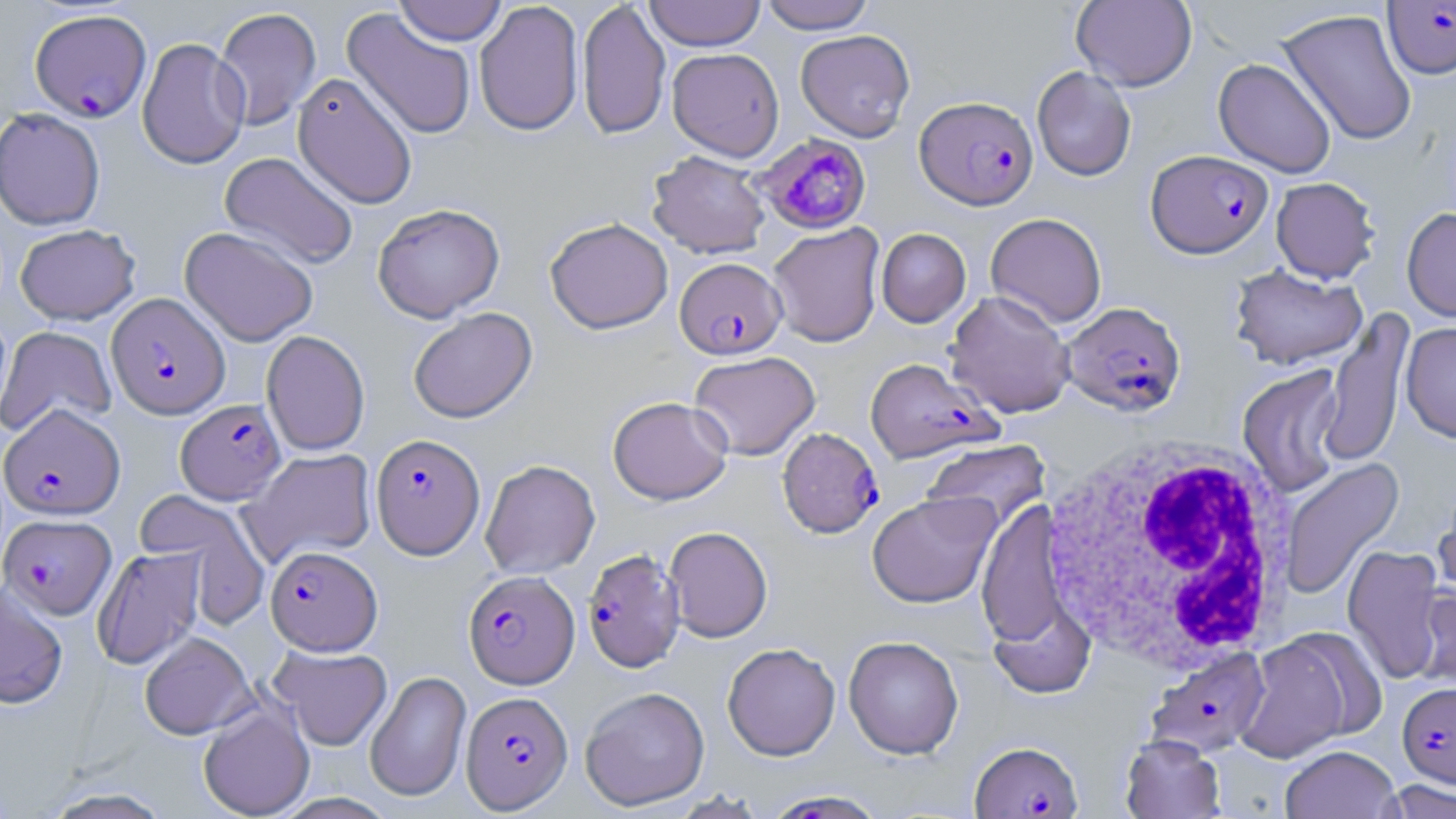 Approximate bounding boxes as [x1, y1, x2, y2] in pixels. White blood cell locations: [1038, 435, 1301, 678]. Uninfected red blood cell locations: [393, 0, 508, 46], [577, 0, 671, 140], [644, 0, 765, 51], [1071, 0, 1198, 91], [759, 1, 876, 33], [473, 2, 583, 137], [213, 6, 322, 131], [341, 7, 477, 140], [1277, 9, 1418, 147], [795, 29, 914, 142], [136, 37, 250, 169], [667, 48, 784, 161], [1214, 58, 1336, 177], [1032, 66, 1136, 181], [292, 72, 417, 209], [0, 108, 106, 230], [647, 150, 770, 259], [219, 152, 359, 271], [1270, 177, 1381, 283], [373, 203, 505, 322], [1402, 207, 1456, 322], [985, 212, 1107, 329], [545, 217, 673, 334], [768, 223, 885, 347], [14, 224, 141, 325], [180, 226, 319, 347], [876, 228, 971, 327], [1229, 264, 1368, 371], [945, 290, 1075, 418], [408, 307, 537, 423], [1316, 309, 1415, 469], [0, 310, 13, 426], [1400, 321, 1456, 443], [0, 326, 117, 438], [261, 330, 370, 456], [689, 350, 820, 460], [1237, 365, 1347, 499], [607, 396, 733, 505], [920, 440, 1050, 536], [240, 449, 376, 567], [1280, 458, 1404, 600], [480, 459, 600, 579], [1433, 487, 1456, 607], [135, 490, 270, 624], [866, 491, 1001, 608], [977, 498, 1070, 651], [664, 526, 773, 642], [1342, 544, 1449, 684], [92, 547, 206, 670], [0, 582, 69, 709], [1414, 582, 1456, 691], [986, 593, 1097, 700], [139, 631, 256, 740], [1235, 633, 1359, 762], [843, 635, 963, 759], [722, 643, 841, 760], [268, 645, 392, 751], [365, 670, 471, 803], [579, 686, 710, 811], [198, 702, 315, 818], [1120, 734, 1226, 818], [1280, 745, 1401, 818], [1378, 779, 1456, 818], [40, 787, 174, 818], [760, 789, 888, 818]. Plasmodium falciparum-infected red blood cell locations: [1383, 1, 1456, 78], [29, 8, 151, 123], [915, 96, 1038, 210], [755, 134, 872, 235], [1146, 150, 1273, 259], [675, 257, 787, 359], [106, 292, 230, 419], [1061, 301, 1186, 416], [864, 357, 1001, 463], [176, 399, 286, 504], [1, 404, 125, 520], [778, 427, 883, 538], [370, 433, 485, 559], [1, 514, 116, 619], [266, 545, 382, 655], [582, 549, 685, 673], [464, 570, 579, 689], [1146, 648, 1271, 758], [1398, 682, 1456, 788], [461, 691, 572, 813], [969, 740, 1083, 818]. Slide-level diagnosis: Plasmodium falciparum. 1000x magnification. Image is 1456×819 pixels. Single field of view. Optical microscopy. Thin blood film. May-Grünwald-Giemsa-stained preparation.